Locate every uninfected red blood cell.
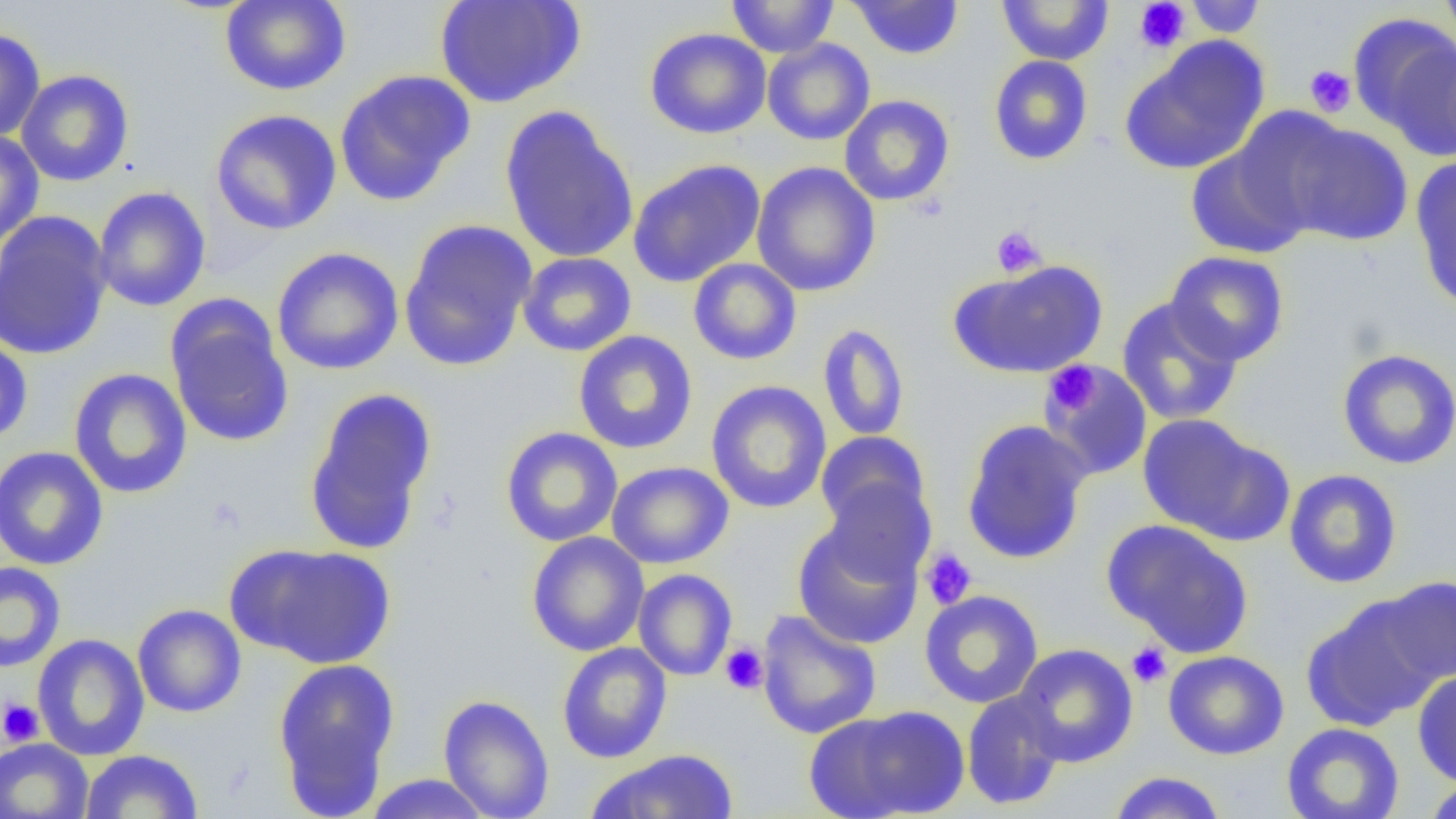
Approximate bounding boxes as (x1, y1, x2, y2) in pixels.
Uninfected red blood cells: (434, 0, 586, 109), (726, 0, 839, 58), (849, 0, 964, 59), (996, 0, 1115, 66), (1183, 0, 1267, 38), (1438, 0, 1456, 50), (220, 1, 352, 96), (1351, 15, 1456, 151), (0, 27, 45, 143), (645, 27, 772, 139), (1120, 37, 1270, 175), (762, 38, 875, 145), (988, 55, 1094, 165), (15, 69, 135, 186), (334, 69, 476, 207), (839, 94, 954, 206), (499, 106, 639, 265), (1223, 106, 1358, 234), (210, 109, 342, 235), (1282, 120, 1412, 247), (0, 130, 44, 248), (1185, 142, 1313, 260), (1411, 156, 1456, 313), (627, 159, 766, 287), (751, 162, 881, 297), (93, 186, 210, 312), (0, 211, 113, 360), (398, 218, 538, 373), (271, 246, 404, 376), (1165, 250, 1290, 366), (517, 252, 637, 356), (687, 258, 802, 365), (950, 259, 1108, 379), (1116, 296, 1244, 425), (166, 299, 294, 449), (817, 323, 910, 442), (573, 330, 698, 454), (0, 334, 33, 446), (1336, 348, 1456, 470), (1039, 360, 1153, 479), (68, 368, 192, 499), (705, 380, 832, 514), (303, 387, 438, 556), (1136, 413, 1275, 541), (960, 419, 1093, 565), (500, 426, 623, 547), (815, 431, 932, 539), (0, 446, 108, 571), (606, 461, 734, 569), (1284, 468, 1402, 588), (820, 477, 935, 583), (792, 517, 925, 650), (1102, 519, 1254, 658), (526, 532, 649, 656), (234, 543, 397, 670), (0, 561, 66, 673), (633, 568, 737, 681), (1378, 576, 1456, 685), (919, 590, 1043, 708), (1302, 597, 1443, 731), (133, 604, 246, 718), (757, 610, 882, 740), (32, 633, 150, 760), (556, 642, 672, 763), (1012, 643, 1138, 767), (1163, 650, 1289, 760), (273, 657, 400, 814), (1412, 671, 1456, 787), (961, 688, 1067, 811), (438, 694, 555, 819), (817, 705, 971, 819), (1281, 722, 1404, 819), (0, 738, 93, 819), (585, 749, 740, 819), (81, 750, 203, 818), (1108, 771, 1227, 819), (362, 773, 494, 818), (1422, 776, 1456, 819).

Platelet locations: (1134, 1, 1190, 53), (1305, 65, 1356, 117), (990, 226, 1046, 278), (1045, 361, 1100, 415), (920, 548, 978, 610), (1127, 642, 1172, 687), (719, 643, 769, 694), (0, 698, 45, 746). Slide-level diagnosis: negative for blood parasites. Captured at 1000x magnification. Thin blood smear. One field of a larger specimen. Light microscopy. Image is 1456×819 pixels.